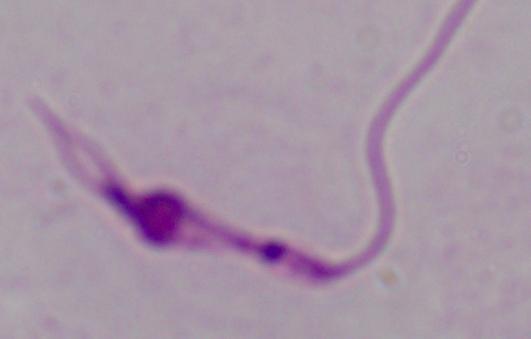

Summary:
  - Magnification: 1000x
  - Modality: micrograph
  - Identification: Leishmania